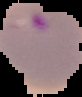
Image is 82×97 pixels. Malaria status: parasitized. Cell region segmented out of the field of view; the surrounding area is masked to black. From a thin blood film.